Name the cell type shown.
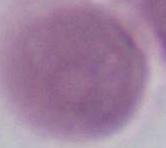

This is an erythrocyte.

Micrograph. 1000x magnification.